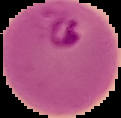
result = malaria parasites identified
preparation = thin blood smear
image type = segmented cell region on a black background
image size = 121×118 pixels